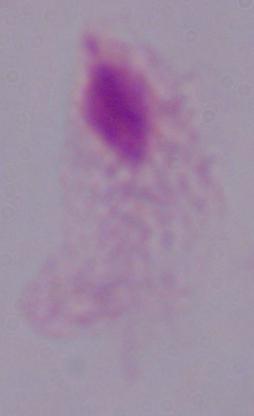
Micrograph. Captured at 1000x magnification. A trichomonad is seen.